Mark where cells are.
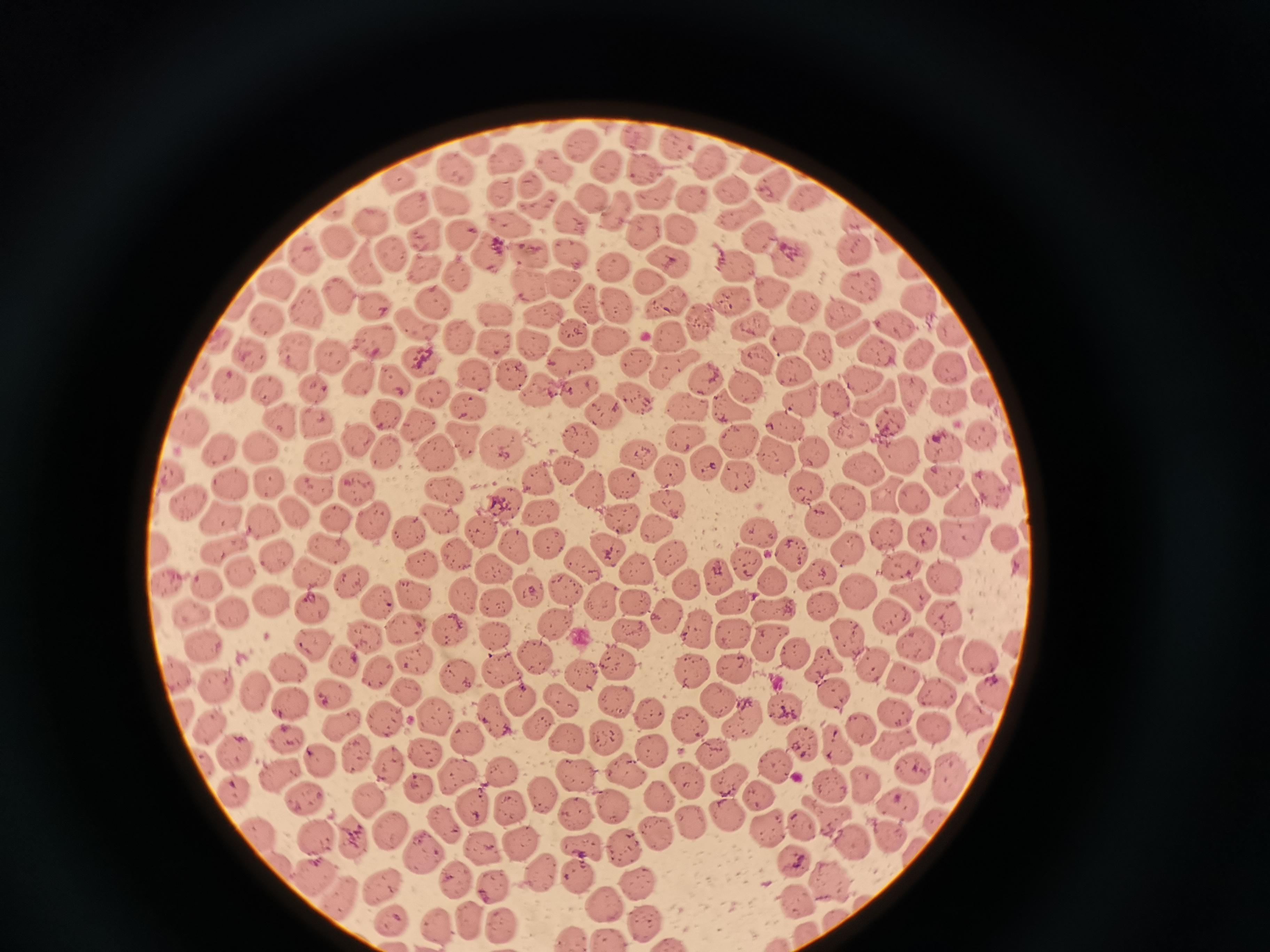
Approximate centers as [x, y] in pixels.
Cells: [637, 136], [583, 142], [677, 142], [473, 144], [506, 158], [755, 159], [709, 161], [455, 165], [605, 165], [552, 167], [641, 170], [398, 180], [530, 182], [776, 185], [731, 188], [499, 192], [654, 194], [809, 196], [593, 197], [452, 198], [691, 201], [537, 204], [412, 209], [617, 210], [570, 215], [859, 216], [371, 221], [508, 223], [647, 228], [463, 229], [679, 231], [763, 237], [424, 239], [890, 240], [337, 244], [571, 247], [855, 248], [530, 251], [305, 254], [486, 255], [395, 256], [793, 257], [367, 261], [670, 261], [737, 265], [612, 266], [915, 266], [421, 268], [457, 271], [528, 279], [278, 282], [861, 282], [650, 283], [561, 285], [775, 292], [341, 293], [732, 300], [920, 300], [434, 302], [666, 302], [372, 303], [589, 304], [617, 304], [306, 305], [497, 309], [807, 309], [839, 310], [268, 313], [543, 316], [698, 319], [896, 322], [417, 323], [750, 326], [956, 327], [854, 332], [575, 334], [220, 336], [666, 337], [373, 338], [458, 338], [497, 339], [612, 339], [790, 341], [528, 344], [820, 347], [295, 350], [880, 350], [247, 352], [329, 353], [918, 353], [422, 357], [756, 357], [570, 361], [634, 363], [675, 368], [954, 369], [797, 371], [471, 373], [512, 373], [198, 374], [357, 376], [864, 377], [707, 378], [396, 381], [229, 385], [746, 385], [311, 386], [266, 387], [577, 389], [538, 390], [430, 391], [912, 391], [985, 395], [836, 397], [875, 398], [946, 398], [634, 399], [801, 401], [731, 406], [467, 407], [686, 408], [386, 410], [601, 410], [280, 420], [317, 420], [888, 420], [785, 423], [419, 425], [190, 427], [849, 432], [685, 434], [984, 435], [358, 437], [461, 439], [736, 439], [502, 445], [581, 446], [940, 447], [264, 449], [434, 450], [773, 450], [218, 451], [638, 453], [899, 453], [388, 454], [816, 454], [325, 456], [705, 463], [672, 469], [865, 470], [566, 472], [1014, 474], [734, 475], [945, 477], [172, 478], [539, 479], [625, 482], [267, 485], [352, 486], [809, 486], [227, 487], [990, 487], [312, 488], [444, 490], [590, 491], [892, 497], [847, 500], [915, 500], [190, 502], [505, 503], [666, 503], [961, 503], [539, 507], [291, 513], [224, 517], [439, 518], [618, 518], [822, 518], [267, 519], [336, 521], [375, 523], [659, 527], [407, 528], [481, 529], [759, 532], [890, 535], [927, 535], [1002, 536], [548, 542], [960, 544], [516, 545], [160, 546], [327, 549], [608, 549], [852, 551], [223, 552], [459, 552], [795, 552], [276, 554], [673, 556], [581, 561], [745, 563], [420, 564], [899, 566], [493, 569], [636, 570], [242, 571], [819, 573], [312, 574], [945, 575], [717, 576], [167, 579], [771, 580], [350, 581], [207, 582], [686, 582], [561, 587], [858, 589], [413, 591], [526, 592], [461, 594], [905, 594], [377, 600], [271, 601], [634, 601], [494, 603], [602, 603], [732, 603], [823, 607], [311, 610], [770, 611], [190, 613], [232, 613], [664, 613], [890, 613], [944, 615], [554, 624], [402, 625], [701, 629], [447, 632], [630, 632], [732, 634], [496, 636], [363, 637], [848, 639], [310, 644], [765, 644], [912, 644], [204, 647], [796, 651], [532, 656], [984, 656], [956, 658], [411, 661], [340, 662], [617, 663], [824, 664], [286, 665], [878, 665], [372, 668], [501, 668], [694, 669], [734, 669], [174, 673], [581, 674], [459, 676], [911, 680], [216, 682], [254, 690], [408, 692], [834, 694], [937, 694], [333, 695], [557, 696], [995, 696], [614, 699], [521, 700], [717, 700], [288, 706], [784, 708], [647, 711], [896, 711], [970, 711], [181, 712], [495, 714], [434, 715], [743, 719], [687, 720], [537, 721], [384, 722], [209, 725], [343, 726], [859, 726], [930, 727], [468, 738], [604, 739], [287, 740], [837, 740], [567, 741], [799, 741], [894, 746], [713, 752], [355, 753], [424, 753], [652, 753], [232, 754], [318, 759], [771, 762], [391, 764], [499, 770], [624, 771], [575, 773], [911, 774], [277, 775], [457, 777], [687, 777], [729, 777], [865, 783], [417, 787], [832, 787], [232, 790], [542, 792], [756, 796], [370, 798], [659, 798], [305, 799], [893, 804], [610, 807], [472, 808], [509, 808], [726, 813], [575, 815], [827, 816], [801, 825], [443, 826], [767, 828], [255, 829], [691, 829], [390, 831], [654, 831], [890, 833], [318, 835], [349, 836], [521, 841], [852, 843], [482, 847], [578, 849], [618, 850], [421, 851], [792, 855], [543, 871], [310, 872], [577, 876], [452, 877], [828, 878], [493, 883], [381, 885], [638, 886], [337, 898], [796, 900], [602, 905], [468, 916], [393, 920], [432, 920], [500, 920], [644, 921], [605, 937], [570, 938].

Photographed with a smartphone camera at the microscope eyepiece. Image is 1270×952 pixels. Thin blood film. Single field of view. Giemsa-stained preparation.